Assess this cell for malaria.
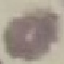
Uninfected.

Thin blood film. Automatically extracted cell patch, resized to 64 × 64 pixels. Giemsa-stained preparation. Photographed with a smartphone camera at the microscope eyepiece.